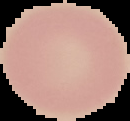 Image is 130×121 pixels. From a thin blood film. Cell region segmented out of the field of view; the surrounding area is masked to black. Malaria status: uninfected.